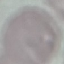
{
  "malaria_status": "uninfected",
  "preparation": "thin smear",
  "stain": "Giemsa",
  "capture": "smartphone camera at the microscope eyepiece",
  "image_type": "automatically extracted cell patch, resized to 64 × 64 pixels"
}